Name the blood parasite species.
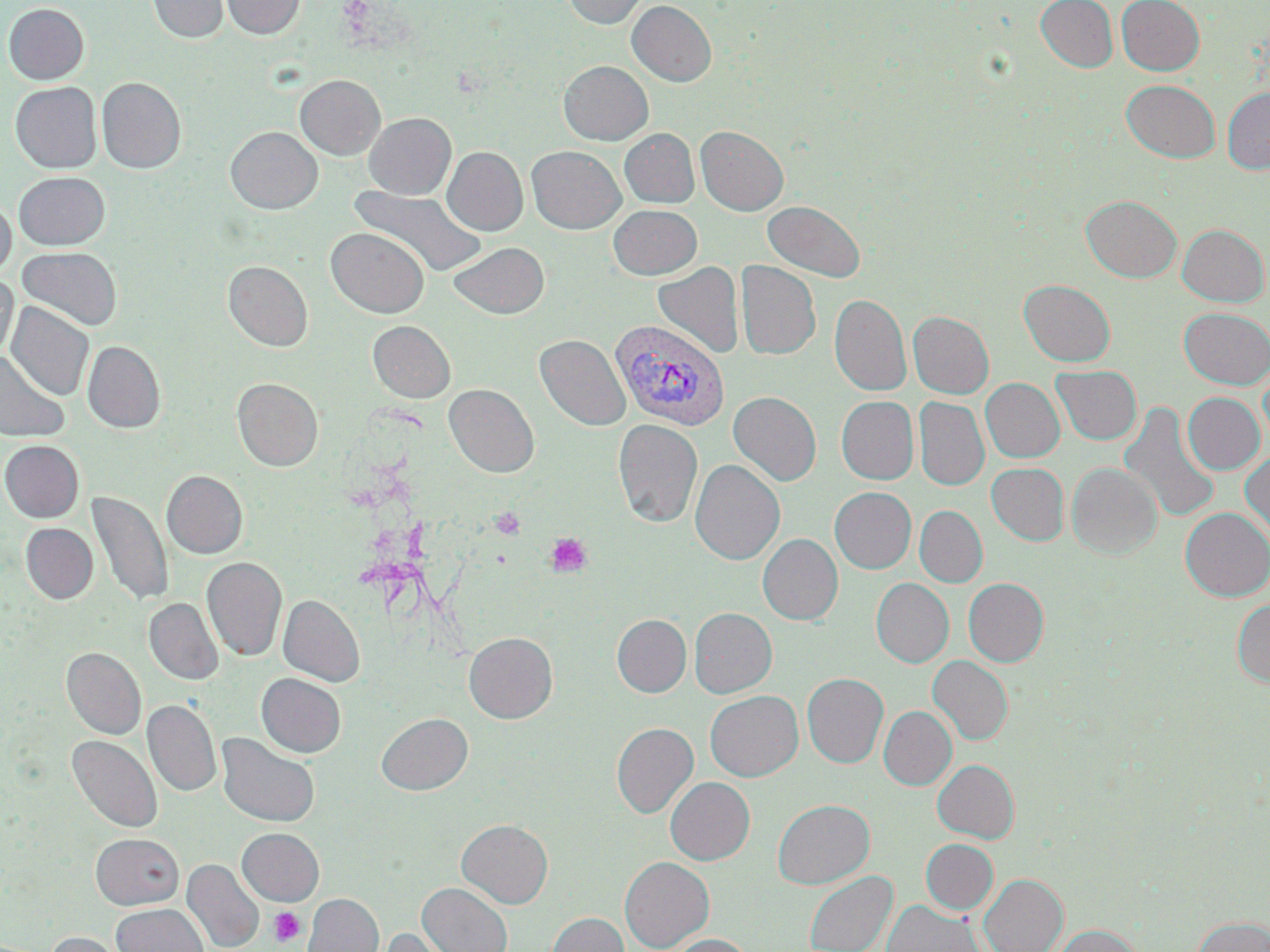

Plasmodium vivax.

Approximate bounding boxes as named x1/y1/x2/y2 corners in pixels. Platelet locations: (x1=489, y1=507, x2=526, y2=540), (x1=546, y1=532, x2=593, y2=578), (x1=269, y1=907, x2=305, y2=946). Uninfected red blood cell locations: (x1=147, y1=0, x2=229, y2=42), (x1=221, y1=0, x2=305, y2=38), (x1=563, y1=0, x2=649, y2=28), (x1=1035, y1=0, x2=1118, y2=72), (x1=1116, y1=0, x2=1205, y2=75), (x1=627, y1=1, x2=716, y2=86), (x1=2, y1=3, x2=89, y2=84), (x1=559, y1=61, x2=653, y2=144), (x1=295, y1=75, x2=385, y2=160), (x1=96, y1=77, x2=186, y2=173), (x1=1121, y1=80, x2=1220, y2=163), (x1=10, y1=82, x2=101, y2=173), (x1=1222, y1=87, x2=1270, y2=174), (x1=364, y1=112, x2=456, y2=199), (x1=695, y1=125, x2=788, y2=215), (x1=225, y1=126, x2=322, y2=214), (x1=620, y1=128, x2=699, y2=207), (x1=527, y1=146, x2=626, y2=233), (x1=442, y1=147, x2=528, y2=235), (x1=14, y1=171, x2=110, y2=250), (x1=351, y1=187, x2=485, y2=277), (x1=1082, y1=195, x2=1182, y2=282), (x1=0, y1=198, x2=16, y2=278), (x1=763, y1=201, x2=865, y2=282), (x1=608, y1=204, x2=702, y2=279), (x1=1177, y1=224, x2=1269, y2=306), (x1=327, y1=228, x2=428, y2=317), (x1=449, y1=241, x2=548, y2=319), (x1=17, y1=247, x2=122, y2=329), (x1=223, y1=260, x2=313, y2=351), (x1=736, y1=261, x2=820, y2=360), (x1=653, y1=262, x2=744, y2=358), (x1=0, y1=274, x2=18, y2=360), (x1=1019, y1=280, x2=1115, y2=366), (x1=830, y1=294, x2=911, y2=396), (x1=6, y1=301, x2=94, y2=401), (x1=1179, y1=307, x2=1270, y2=389), (x1=908, y1=311, x2=993, y2=398), (x1=368, y1=321, x2=455, y2=402), (x1=535, y1=334, x2=630, y2=431), (x1=83, y1=341, x2=165, y2=432), (x1=0, y1=353, x2=69, y2=442), (x1=1258, y1=362, x2=1270, y2=450), (x1=1051, y1=365, x2=1142, y2=445), (x1=232, y1=377, x2=323, y2=470), (x1=981, y1=378, x2=1065, y2=462), (x1=444, y1=384, x2=539, y2=477), (x1=728, y1=391, x2=822, y2=486), (x1=1183, y1=392, x2=1265, y2=474), (x1=836, y1=396, x2=919, y2=484), (x1=914, y1=397, x2=989, y2=490), (x1=1119, y1=402, x2=1221, y2=524), (x1=613, y1=419, x2=703, y2=528), (x1=0, y1=440, x2=84, y2=522), (x1=13, y1=440, x2=90, y2=603), (x1=1240, y1=450, x2=1270, y2=543), (x1=690, y1=459, x2=785, y2=565), (x1=986, y1=463, x2=1069, y2=545), (x1=1067, y1=463, x2=1161, y2=558), (x1=162, y1=470, x2=247, y2=558), (x1=829, y1=487, x2=916, y2=573), (x1=87, y1=491, x2=172, y2=607), (x1=914, y1=506, x2=987, y2=587), (x1=1180, y1=507, x2=1270, y2=601), (x1=20, y1=523, x2=97, y2=603), (x1=758, y1=534, x2=843, y2=625), (x1=202, y1=557, x2=287, y2=661), (x1=871, y1=578, x2=954, y2=667), (x1=963, y1=578, x2=1049, y2=666), (x1=278, y1=594, x2=364, y2=686), (x1=144, y1=598, x2=223, y2=685), (x1=1231, y1=599, x2=1270, y2=686), (x1=689, y1=608, x2=777, y2=698), (x1=612, y1=614, x2=691, y2=697), (x1=464, y1=631, x2=558, y2=723), (x1=61, y1=647, x2=146, y2=739), (x1=928, y1=656, x2=1013, y2=745), (x1=256, y1=673, x2=346, y2=758), (x1=802, y1=673, x2=888, y2=767), (x1=705, y1=690, x2=803, y2=781), (x1=143, y1=700, x2=221, y2=796), (x1=879, y1=706, x2=956, y2=790), (x1=376, y1=712, x2=472, y2=795), (x1=612, y1=722, x2=699, y2=817), (x1=216, y1=733, x2=320, y2=827), (x1=67, y1=736, x2=162, y2=833), (x1=933, y1=759, x2=1019, y2=842), (x1=665, y1=777, x2=755, y2=865), (x1=772, y1=799, x2=874, y2=888), (x1=457, y1=819, x2=553, y2=908), (x1=237, y1=828, x2=323, y2=905), (x1=90, y1=833, x2=184, y2=909), (x1=921, y1=839, x2=998, y2=914), (x1=620, y1=856, x2=714, y2=951), (x1=182, y1=859, x2=264, y2=952), (x1=804, y1=871, x2=897, y2=952), (x1=979, y1=874, x2=1067, y2=952), (x1=418, y1=883, x2=512, y2=952), (x1=302, y1=893, x2=383, y2=952), (x1=882, y1=900, x2=985, y2=952), (x1=112, y1=904, x2=207, y2=952), (x1=547, y1=912, x2=629, y2=952), (x1=1192, y1=916, x2=1270, y2=952), (x1=1053, y1=924, x2=1143, y2=952), (x1=372, y1=926, x2=459, y2=952), (x1=44, y1=932, x2=130, y2=952), (x1=668, y1=934, x2=754, y2=952). Plasmodium vivax-infected red blood cell locations: (x1=612, y1=320, x2=730, y2=431). Image is 1270×952 pixels. One field of a larger specimen. Optical microscopy. 1000x magnification. Thin blood smear. May-Grünwald-Giemsa stain.